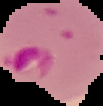
malaria_status: parasitized
image_type: segmented cell region with the area outside set to black
preparation: thin blood smear
image_size: 103×106 pixels